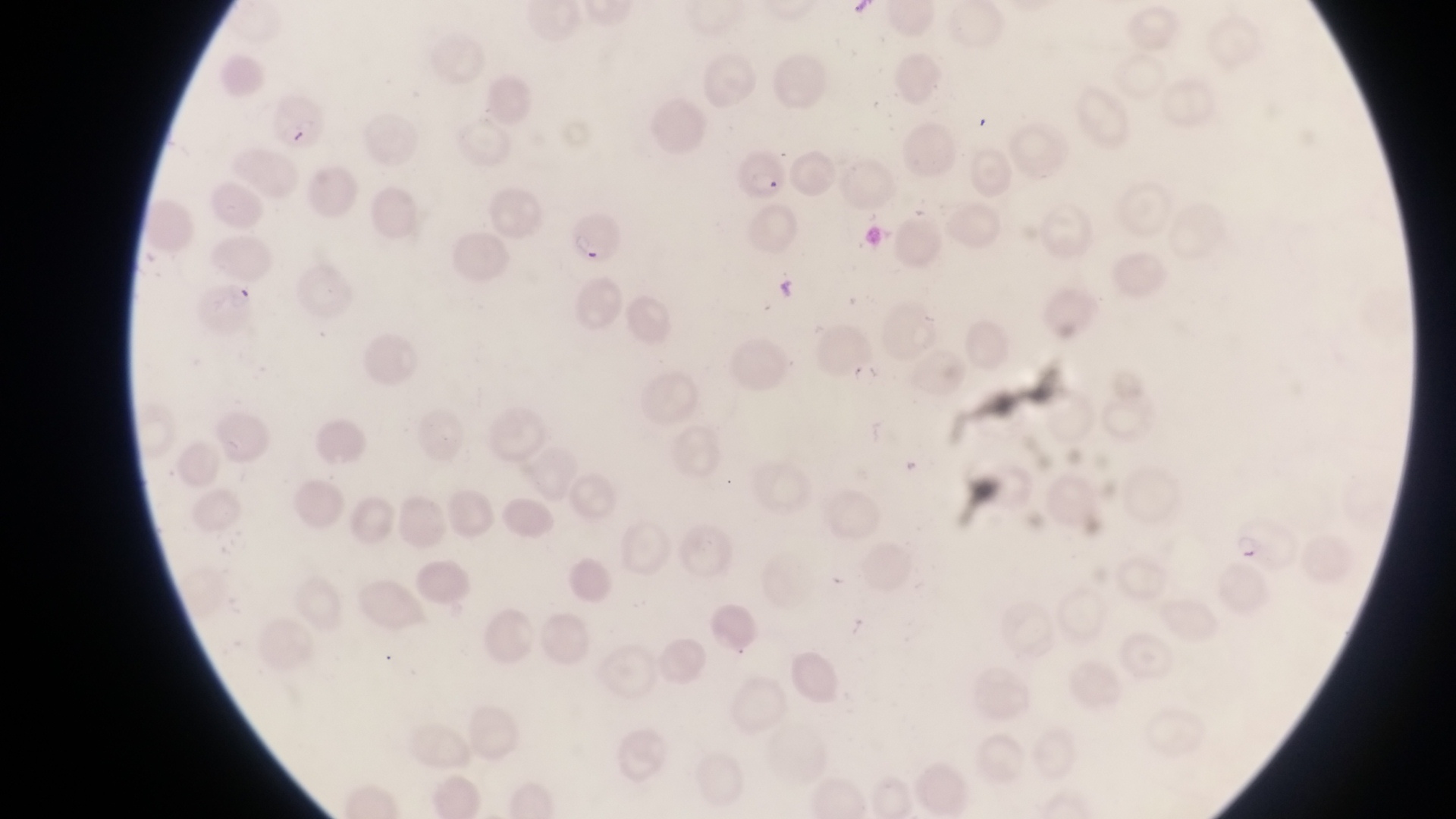
Approximate bounding boxes as [left, top, right, bottom] in pixels.
Summary:
  - Parasitised red blood cell locations: [265, 95, 329, 156], [730, 139, 790, 200], [566, 206, 625, 262], [191, 283, 260, 341], [1238, 516, 1298, 568]
  - Preparation: thin blood film
  - Capture: smartphone photograph through the eyepiece of an Olympus CX-23 microscope
  - Image size: 1456×819 pixels
  - Field of view: single
  - Magnification: 1000x
  - Country: Uganda